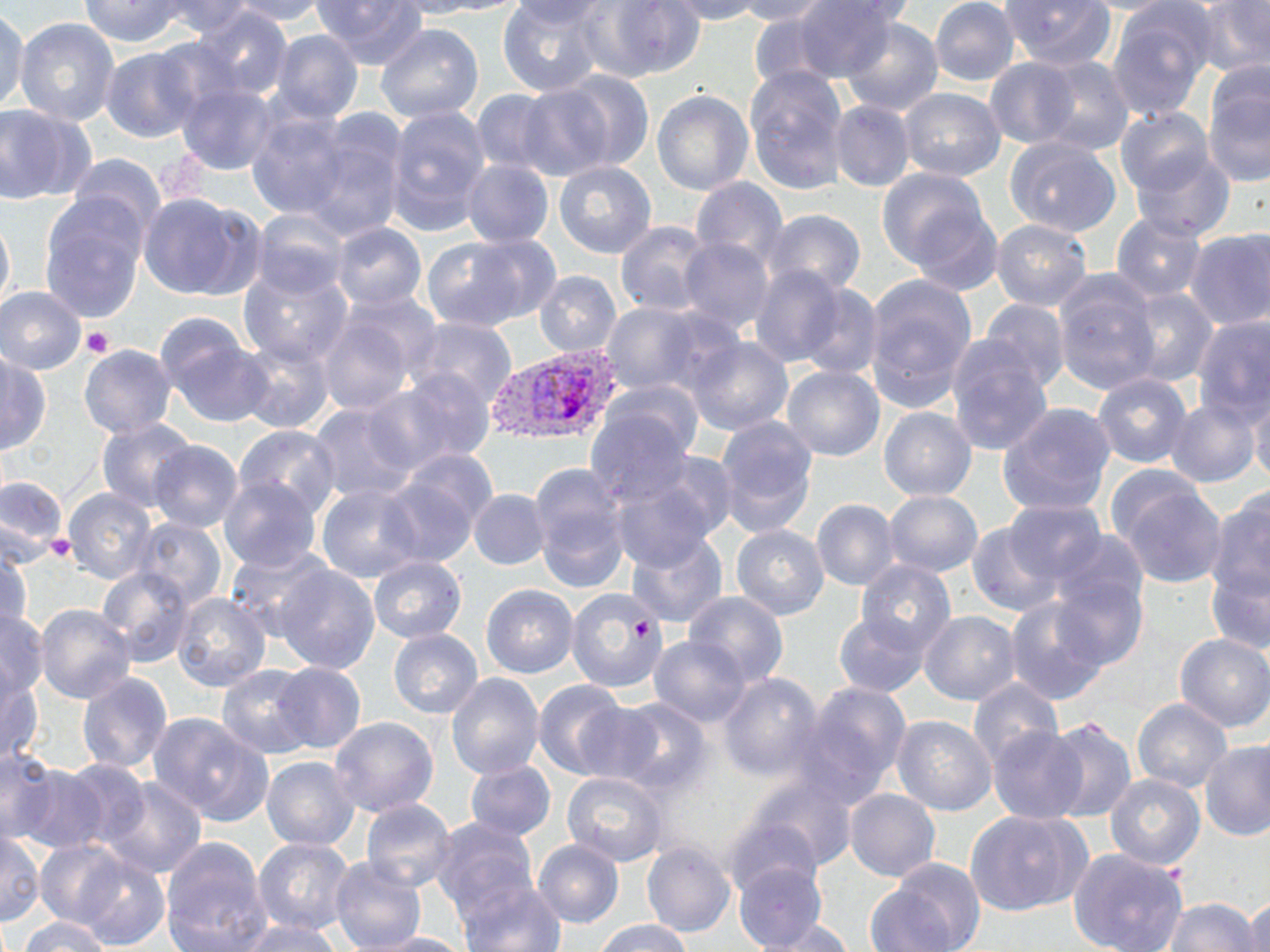
Summary:
  - Coordinate format: approximate bounding boxes as named x1/y1/x2/y2 corners in pixels
  - Platelet locations: (x1=81, y1=326, x2=114, y2=358), (x1=44, y1=534, x2=74, y2=563)
  - Uninfected red blood cell locations: (x1=153, y1=0, x2=257, y2=37), (x1=220, y1=0, x2=332, y2=25), (x1=311, y1=0, x2=428, y2=70), (x1=382, y1=0, x2=491, y2=19), (x1=413, y1=0, x2=531, y2=15), (x1=498, y1=0, x2=604, y2=96), (x1=591, y1=0, x2=704, y2=81), (x1=664, y1=0, x2=771, y2=24), (x1=731, y1=0, x2=838, y2=26), (x1=788, y1=0, x2=899, y2=82), (x1=805, y1=0, x2=922, y2=27), (x1=929, y1=0, x2=1020, y2=87), (x1=999, y1=0, x2=1116, y2=71), (x1=1193, y1=0, x2=1270, y2=77), (x1=79, y1=1, x2=190, y2=48), (x1=507, y1=1, x2=612, y2=27), (x1=1068, y1=1, x2=1189, y2=15), (x1=1106, y1=2, x2=1215, y2=120), (x1=0, y1=5, x2=29, y2=116), (x1=189, y1=5, x2=292, y2=101), (x1=746, y1=5, x2=855, y2=91), (x1=840, y1=16, x2=944, y2=116), (x1=15, y1=19, x2=120, y2=126), (x1=375, y1=24, x2=484, y2=122), (x1=269, y1=29, x2=363, y2=123), (x1=101, y1=47, x2=203, y2=143), (x1=1030, y1=55, x2=1135, y2=156), (x1=982, y1=58, x2=1083, y2=149), (x1=743, y1=66, x2=849, y2=194), (x1=545, y1=70, x2=656, y2=172), (x1=1017, y1=78, x2=1132, y2=209), (x1=1202, y1=80, x2=1270, y2=186), (x1=176, y1=84, x2=279, y2=176), (x1=514, y1=84, x2=617, y2=180), (x1=471, y1=88, x2=563, y2=175), (x1=652, y1=89, x2=755, y2=195), (x1=898, y1=89, x2=1006, y2=182), (x1=829, y1=100, x2=914, y2=193), (x1=0, y1=104, x2=89, y2=204), (x1=384, y1=105, x2=491, y2=231), (x1=1113, y1=106, x2=1217, y2=196), (x1=244, y1=110, x2=352, y2=218), (x1=301, y1=119, x2=409, y2=240), (x1=1004, y1=136, x2=1123, y2=236), (x1=1130, y1=149, x2=1235, y2=240), (x1=67, y1=153, x2=165, y2=239), (x1=462, y1=159, x2=553, y2=247), (x1=554, y1=160, x2=656, y2=258), (x1=877, y1=167, x2=991, y2=271), (x1=689, y1=177, x2=789, y2=268), (x1=138, y1=193, x2=259, y2=300), (x1=39, y1=197, x2=148, y2=322), (x1=903, y1=202, x2=1002, y2=294), (x1=251, y1=208, x2=349, y2=299), (x1=760, y1=208, x2=867, y2=295), (x1=0, y1=210, x2=14, y2=321), (x1=1111, y1=212, x2=1207, y2=300), (x1=991, y1=219, x2=1092, y2=309), (x1=615, y1=220, x2=713, y2=316), (x1=331, y1=223, x2=427, y2=311), (x1=1185, y1=227, x2=1270, y2=330), (x1=422, y1=233, x2=552, y2=331), (x1=676, y1=237, x2=776, y2=335), (x1=749, y1=262, x2=849, y2=367), (x1=238, y1=265, x2=353, y2=366), (x1=534, y1=271, x2=622, y2=357), (x1=864, y1=274, x2=977, y2=400), (x1=1053, y1=275, x2=1159, y2=394), (x1=797, y1=281, x2=884, y2=379), (x1=1118, y1=287, x2=1218, y2=387), (x1=0, y1=288, x2=88, y2=375), (x1=313, y1=298, x2=436, y2=415), (x1=978, y1=298, x2=1072, y2=392), (x1=598, y1=301, x2=732, y2=397), (x1=1192, y1=314, x2=1270, y2=423), (x1=155, y1=317, x2=269, y2=426), (x1=409, y1=318, x2=518, y2=411), (x1=684, y1=336, x2=794, y2=436), (x1=237, y1=337, x2=336, y2=435), (x1=944, y1=341, x2=1055, y2=458), (x1=79, y1=345, x2=176, y2=439), (x1=0, y1=352, x2=50, y2=454), (x1=782, y1=365, x2=885, y2=462), (x1=377, y1=370, x2=497, y2=470), (x1=1092, y1=373, x2=1193, y2=468), (x1=600, y1=379, x2=706, y2=460), (x1=1246, y1=390, x2=1270, y2=488), (x1=1164, y1=397, x2=1261, y2=488), (x1=306, y1=399, x2=422, y2=503), (x1=998, y1=402, x2=1117, y2=514), (x1=878, y1=405, x2=975, y2=500), (x1=584, y1=408, x2=694, y2=506), (x1=714, y1=414, x2=820, y2=535), (x1=96, y1=417, x2=199, y2=512), (x1=234, y1=424, x2=342, y2=517), (x1=149, y1=441, x2=243, y2=532), (x1=397, y1=449, x2=500, y2=532), (x1=611, y1=464, x2=728, y2=569), (x1=379, y1=468, x2=485, y2=566), (x1=537, y1=470, x2=631, y2=587), (x1=1108, y1=475, x2=1226, y2=589), (x1=0, y1=477, x2=69, y2=564), (x1=218, y1=477, x2=322, y2=572), (x1=316, y1=483, x2=425, y2=582), (x1=63, y1=488, x2=158, y2=583), (x1=469, y1=489, x2=551, y2=570), (x1=884, y1=490, x2=982, y2=577), (x1=1206, y1=490, x2=1270, y2=605), (x1=811, y1=499, x2=900, y2=591), (x1=1002, y1=500, x2=1107, y2=588), (x1=132, y1=517, x2=227, y2=611), (x1=965, y1=521, x2=1060, y2=615), (x1=730, y1=524, x2=829, y2=619), (x1=624, y1=528, x2=728, y2=629), (x1=1049, y1=532, x2=1150, y2=620), (x1=0, y1=545, x2=32, y2=641), (x1=224, y1=545, x2=334, y2=642), (x1=369, y1=556, x2=467, y2=643), (x1=855, y1=559, x2=955, y2=654), (x1=1206, y1=562, x2=1270, y2=654), (x1=273, y1=564, x2=380, y2=672), (x1=98, y1=565, x2=194, y2=667), (x1=1048, y1=572, x2=1148, y2=671), (x1=481, y1=584, x2=579, y2=678), (x1=566, y1=588, x2=669, y2=694), (x1=684, y1=592, x2=789, y2=685), (x1=170, y1=593, x2=272, y2=692), (x1=1005, y1=596, x2=1109, y2=706), (x1=35, y1=604, x2=135, y2=705), (x1=0, y1=608, x2=48, y2=700), (x1=834, y1=610, x2=930, y2=696), (x1=920, y1=611, x2=1021, y2=705), (x1=388, y1=628, x2=483, y2=718), (x1=1175, y1=633, x2=1270, y2=732), (x1=648, y1=635, x2=749, y2=726), (x1=270, y1=662, x2=367, y2=756), (x1=217, y1=664, x2=318, y2=757), (x1=0, y1=671, x2=43, y2=764), (x1=76, y1=672, x2=171, y2=775), (x1=717, y1=672, x2=824, y2=780), (x1=447, y1=674, x2=545, y2=779), (x1=968, y1=677, x2=1064, y2=768), (x1=533, y1=679, x2=629, y2=779), (x1=800, y1=681, x2=912, y2=795), (x1=567, y1=698, x2=667, y2=786), (x1=608, y1=698, x2=713, y2=797), (x1=1132, y1=698, x2=1231, y2=792), (x1=149, y1=713, x2=273, y2=826), (x1=892, y1=715, x2=997, y2=816), (x1=328, y1=716, x2=439, y2=818), (x1=1044, y1=718, x2=1137, y2=820), (x1=987, y1=726, x2=1088, y2=822), (x1=1199, y1=741, x2=1270, y2=841), (x1=0, y1=749, x2=64, y2=846), (x1=262, y1=755, x2=361, y2=851), (x1=54, y1=758, x2=154, y2=849), (x1=8, y1=760, x2=108, y2=853), (x1=464, y1=760, x2=556, y2=841), (x1=561, y1=772, x2=668, y2=866), (x1=1104, y1=774, x2=1204, y2=870), (x1=97, y1=775, x2=208, y2=879), (x1=744, y1=777, x2=858, y2=872), (x1=844, y1=788, x2=940, y2=882), (x1=360, y1=799, x2=457, y2=891), (x1=965, y1=809, x2=1090, y2=916), (x1=720, y1=811, x2=828, y2=900), (x1=430, y1=816, x2=539, y2=917), (x1=0, y1=832, x2=44, y2=927), (x1=253, y1=837, x2=357, y2=934), (x1=159, y1=838, x2=273, y2=952), (x1=37, y1=841, x2=129, y2=928), (x1=534, y1=841, x2=623, y2=927), (x1=642, y1=841, x2=736, y2=937), (x1=1069, y1=847, x2=1188, y2=952), (x1=72, y1=852, x2=170, y2=951), (x1=329, y1=858, x2=426, y2=951), (x1=734, y1=861, x2=829, y2=950), (x1=458, y1=877, x2=566, y2=952), (x1=864, y1=878, x2=966, y2=952), (x1=1243, y1=896, x2=1269, y2=950), (x1=1163, y1=899, x2=1263, y2=951), (x1=20, y1=916, x2=112, y2=952), (x1=593, y1=919, x2=696, y2=951), (x1=755, y1=919, x2=853, y2=952), (x1=234, y1=921, x2=344, y2=951), (x1=361, y1=931, x2=474, y2=952)
  - Plasmodium vivax-infected red blood cell locations: (x1=484, y1=342, x2=626, y2=444)
  - Slide-level diagnosis: Plasmodium vivax
  - Modality: optical microscopy
  - Preparation: thin blood smear
  - Image size: 1270×952 pixels
  - Field of view: single
  - Magnification: 1000x
  - Stain: May-Grünwald-Giemsa